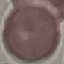

result = no malaria parasites seen
preparation = thin blood smear
capture = smartphone through the microscope eyepiece
stain = Giemsa
image type = cell patch, automatically extracted from a larger field of view and resized to 64 × 64 pixels